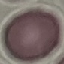
malaria status = uninfected
preparation = thin blood film
stain = Giemsa
capture = smartphone through the microscope eyepiece
image type = automatically extracted cell patch, resized to 64 × 64 pixels